Point out each Plasmodium parasite.
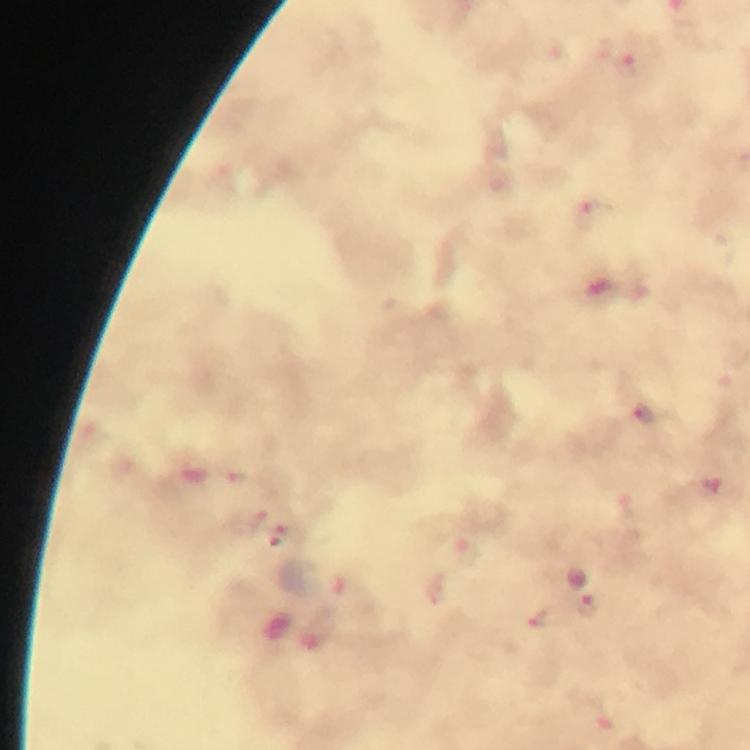
Approximate centers as {x, y} in pixels.
Plasmodium parasites: {629, 67}, {596, 215}, {644, 417}, {256, 522}, {290, 537}, {588, 606}, {545, 619}.

Summary:
  - Cropped from: a single field of view
  - Magnification: 100x
  - Context: from a malaria diagnostic workup
  - Capture: smartphone camera through the microscope
  - Image size: 750×750 pixels
  - Immersion oil: used
  - Stain: Giemsa
  - Preparation: thick smear